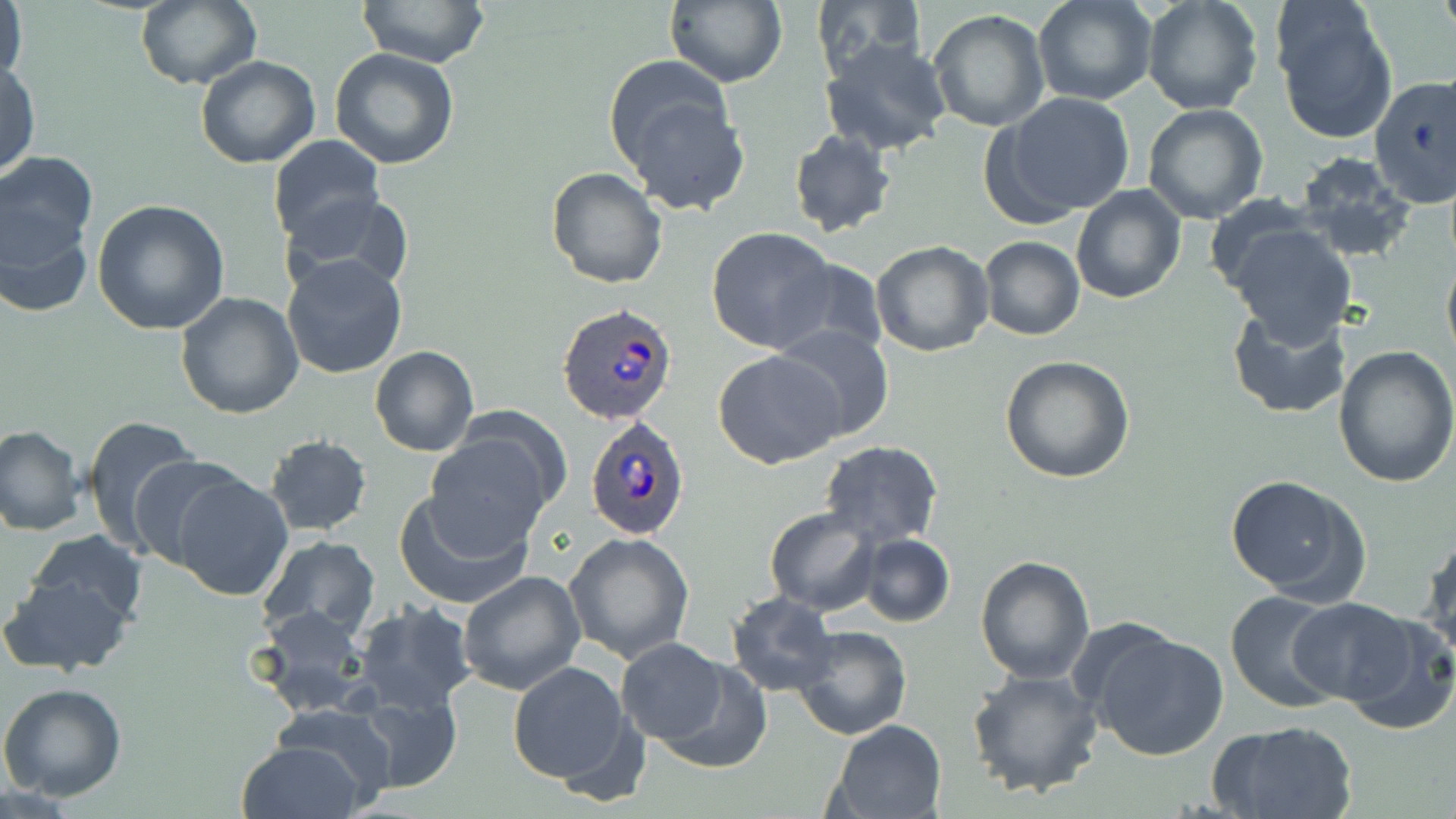
Approximate bounding boxes as named x1/y1/x2/y2 corners in pixels. Plasmodium ovale-infected red blood cell locations: (x1=558, y1=303, x2=680, y2=427), (x1=585, y1=416, x2=691, y2=539). Uninfected red blood cell locations: (x1=1, y1=0, x2=27, y2=93), (x1=663, y1=0, x2=786, y2=89), (x1=1033, y1=0, x2=1158, y2=107), (x1=1139, y1=0, x2=1264, y2=115), (x1=1270, y1=0, x2=1397, y2=144), (x1=359, y1=1, x2=489, y2=69), (x1=809, y1=1, x2=925, y2=79), (x1=134, y1=2, x2=262, y2=89), (x1=928, y1=9, x2=1051, y2=134), (x1=820, y1=37, x2=952, y2=156), (x1=329, y1=48, x2=459, y2=170), (x1=195, y1=56, x2=321, y2=169), (x1=1, y1=60, x2=40, y2=179), (x1=605, y1=64, x2=749, y2=215), (x1=1369, y1=74, x2=1456, y2=208), (x1=991, y1=92, x2=1136, y2=222), (x1=1143, y1=103, x2=1269, y2=224), (x1=788, y1=128, x2=897, y2=238), (x1=268, y1=135, x2=385, y2=250), (x1=0, y1=150, x2=101, y2=278), (x1=1294, y1=157, x2=1416, y2=260), (x1=546, y1=167, x2=667, y2=289), (x1=1070, y1=184, x2=1187, y2=304), (x1=285, y1=192, x2=415, y2=296), (x1=92, y1=199, x2=230, y2=335), (x1=1, y1=203, x2=94, y2=319), (x1=1226, y1=224, x2=1356, y2=345), (x1=705, y1=227, x2=840, y2=354), (x1=980, y1=237, x2=1085, y2=340), (x1=870, y1=240, x2=995, y2=357), (x1=1442, y1=251, x2=1456, y2=369), (x1=282, y1=254, x2=408, y2=380), (x1=773, y1=258, x2=889, y2=362), (x1=174, y1=292, x2=304, y2=420), (x1=1227, y1=306, x2=1351, y2=420), (x1=771, y1=325, x2=896, y2=444), (x1=1333, y1=346, x2=1456, y2=488), (x1=369, y1=347, x2=479, y2=458), (x1=713, y1=349, x2=844, y2=468), (x1=1000, y1=354, x2=1135, y2=484), (x1=78, y1=416, x2=205, y2=554), (x1=425, y1=422, x2=562, y2=547), (x1=0, y1=425, x2=86, y2=535), (x1=264, y1=434, x2=372, y2=536), (x1=821, y1=440, x2=944, y2=548), (x1=127, y1=455, x2=251, y2=569), (x1=165, y1=470, x2=293, y2=601), (x1=1226, y1=476, x2=1369, y2=604), (x1=394, y1=487, x2=536, y2=610), (x1=764, y1=508, x2=880, y2=614), (x1=1420, y1=529, x2=1455, y2=666), (x1=27, y1=530, x2=147, y2=629), (x1=563, y1=532, x2=694, y2=664), (x1=858, y1=534, x2=954, y2=628), (x1=257, y1=536, x2=381, y2=643), (x1=974, y1=555, x2=1094, y2=685), (x1=458, y1=569, x2=586, y2=696), (x1=0, y1=574, x2=135, y2=678), (x1=1225, y1=590, x2=1345, y2=712), (x1=727, y1=592, x2=839, y2=696), (x1=1287, y1=598, x2=1423, y2=708), (x1=352, y1=600, x2=477, y2=714), (x1=255, y1=605, x2=371, y2=714), (x1=1330, y1=605, x2=1456, y2=734), (x1=790, y1=625, x2=912, y2=740), (x1=1087, y1=628, x2=1231, y2=760), (x1=617, y1=638, x2=731, y2=744), (x1=645, y1=655, x2=772, y2=772), (x1=507, y1=661, x2=635, y2=785), (x1=966, y1=669, x2=1103, y2=797), (x1=0, y1=682, x2=128, y2=803), (x1=350, y1=686, x2=464, y2=792), (x1=270, y1=704, x2=401, y2=808), (x1=827, y1=719, x2=946, y2=819), (x1=1209, y1=720, x2=1359, y2=819), (x1=235, y1=739, x2=368, y2=819). Slide-level diagnosis: Plasmodium ovale. May-Grünwald-Giemsa-stained preparation. Optical microscopy. Image is 1456×819 pixels. Captured at 1000x magnification. Single field of view. Thin blood smear.